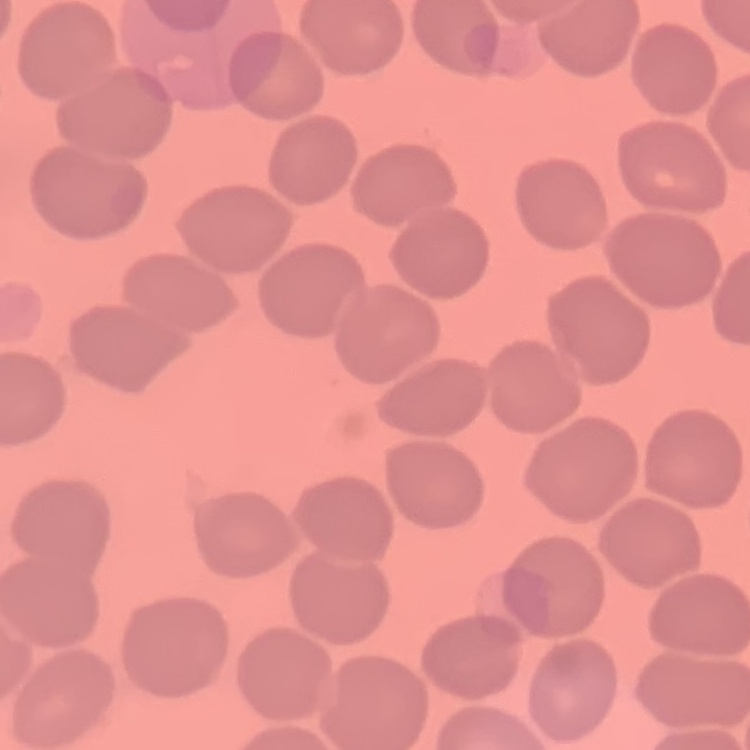
Summary:
  - Erythrocyte morphology: no rouleaux formation
  - Preparation: thin blood smear
  - Image type: square crop of a larger photomicrograph
  - Stain: Field's or Giemsa